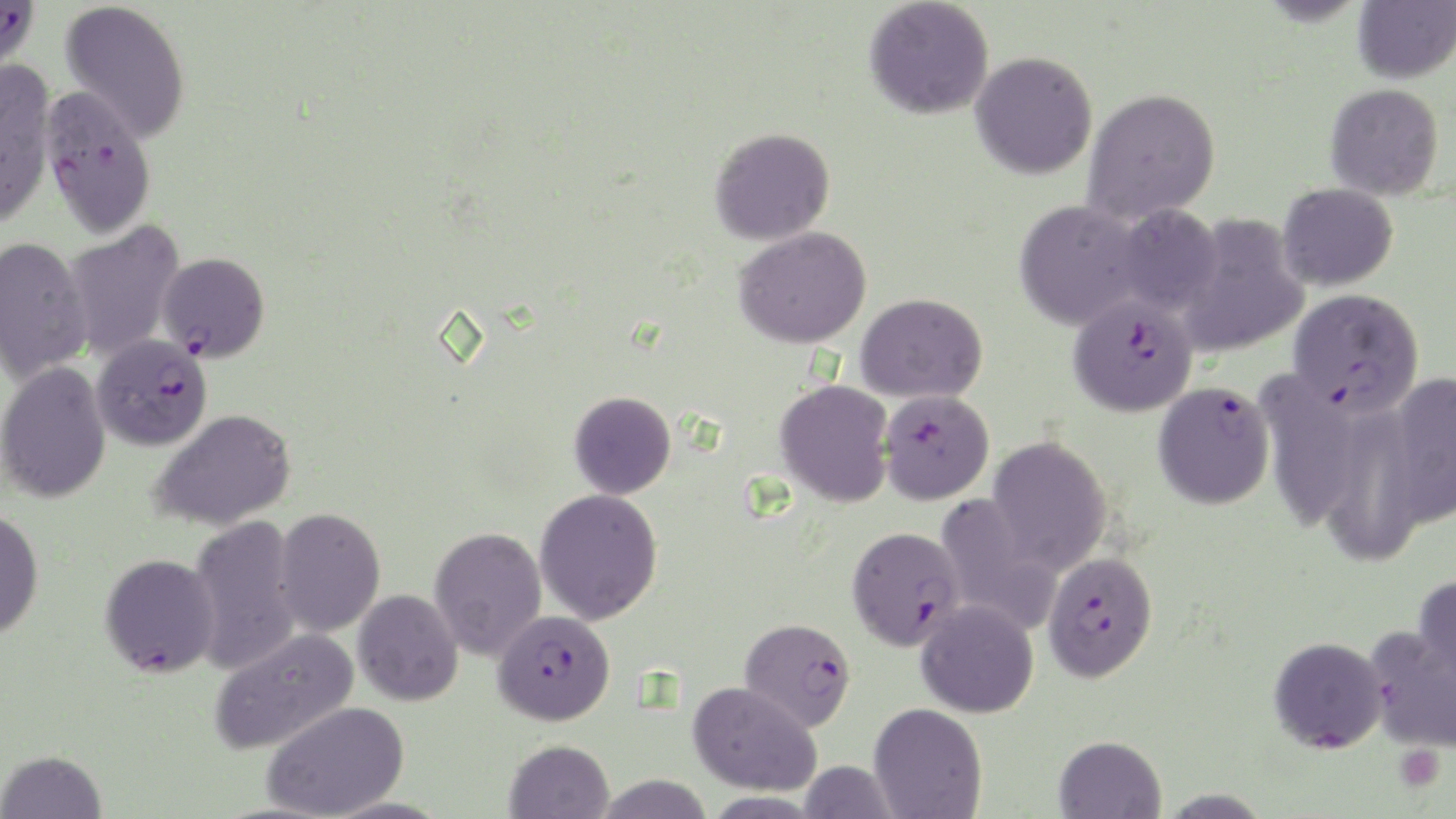
Approximate bounding boxes as (x1,y1)-(x2,y2) corner pairs in pixels. Platelet locations: (1395,745)-(1444,790). Uninfected red blood cell locations: (864,0)-(994,120), (1352,0)-(1455,84), (59,1)-(190,143), (970,51)-(1097,180), (0,58)-(57,227), (1324,83)-(1445,200), (1083,88)-(1221,224), (709,127)-(835,245), (1277,183)-(1398,291), (1014,200)-(1144,331), (1113,204)-(1223,315), (1174,215)-(1309,359), (61,221)-(186,363), (734,226)-(872,348), (0,236)-(92,384), (856,293)-(987,403), (0,361)-(111,504), (1258,373)-(1363,532), (1381,373)-(1456,531), (774,379)-(895,508), (569,391)-(676,499), (1325,405)-(1423,569), (150,408)-(298,532), (987,436)-(1112,574), (534,488)-(663,625), (934,494)-(1061,634), (273,507)-(386,637), (0,509)-(44,639), (188,515)-(300,675), (429,526)-(547,661), (1413,575)-(1456,696), (353,589)-(463,706), (916,599)-(1039,717), (1365,626)-(1456,753), (209,627)-(359,754), (1269,636)-(1388,753), (687,681)-(821,796), (261,701)-(409,819), (869,703)-(988,819), (1053,735)-(1166,819), (503,739)-(614,819), (0,749)-(107,818), (799,760)-(899,818), (594,774)-(714,819), (1155,789)-(1276,816). Plasmodium falciparum-infected red blood cell locations: (0,0)-(39,75), (38,85)-(157,239), (157,252)-(269,361), (1288,287)-(1424,417), (1068,293)-(1198,417), (92,334)-(212,450), (1152,381)-(1275,509), (878,389)-(994,504), (847,526)-(966,651), (1042,551)-(1158,682), (100,553)-(221,678), (492,610)-(616,726), (739,617)-(856,733). Slide-level diagnosis: Plasmodium falciparum. Captured at 1000x magnification. Image is 1456×819 pixels. Optical microscopy. May-Grünwald-Giemsa stain. Single field of view. Thin blood film.